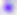
Summary:
  - Identification: Toxoplasma gondii
  - Magnification: 400x
  - Modality: photomicrograph